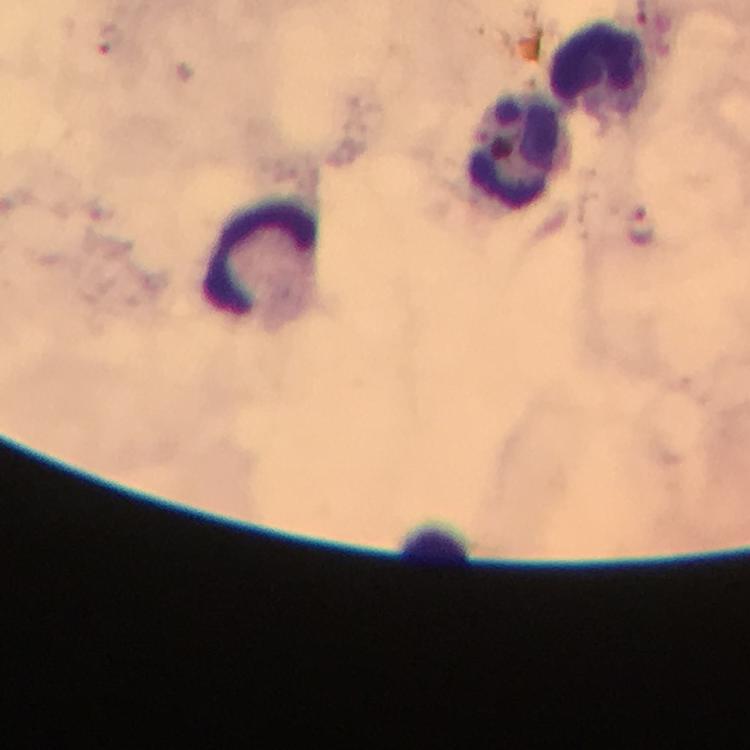

Approximate centers as {x, y} in pixels. Leukocyte locations: {600, 67}, {514, 152}, {263, 256}, {438, 540}. Malaria parasite locations: {109, 38}, {641, 225}. Giemsa-stained preparation. At 100x magnification. Immersion oil was used. Thick blood smear. From a diagnostic examination for malaria. A crop from one field of view. Photographed with a smartphone mounted on the microscope. Image is 750×750 pixels.